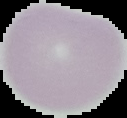
Summary:
  - Result: no malaria parasites seen
  - Preparation: thin blood smear
  - Image size: 127×118 pixels
  - Image type: segmented cell region with the area outside set to black